Describe the morphology of the erythrocytes.
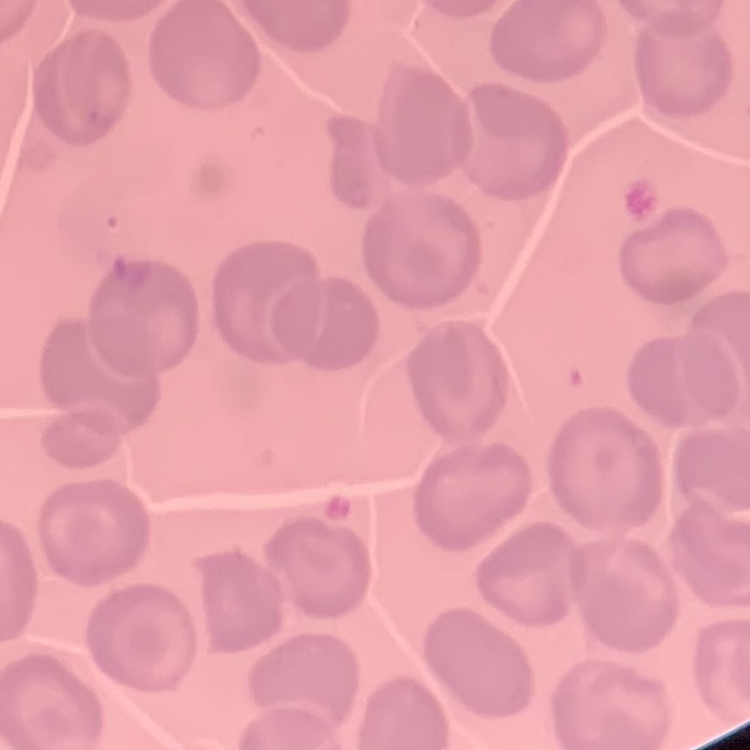
They show no rouleaux formation.

Thin blood film. Field's or Giemsa stain. One tile cut from a larger photomicrograph.